Assess this cell for malaria.
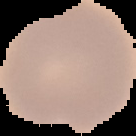

Uninfected.

From a thin blood smear. Image is 136×136 pixels. Segmented cell region on a black background.